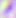
Toxoplasma gondii is shown. 400x magnification. Photomicrograph.